Classify this cell by malaria status.
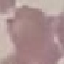

Uninfected.

preparation = thin blood smear
capture = smartphone through the microscope eyepiece
stain = Giemsa
image type = automatically extracted cell patch, resized to 64 × 64 pixels